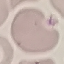

malaria status = uninfected
preparation = thin smear
stain = Giemsa
image type = cell patch, automatically extracted from a larger field of view and resized to 64 × 64 pixels
capture = smartphone camera at the microscope eyepiece